Locate every Plasmodium parasite.
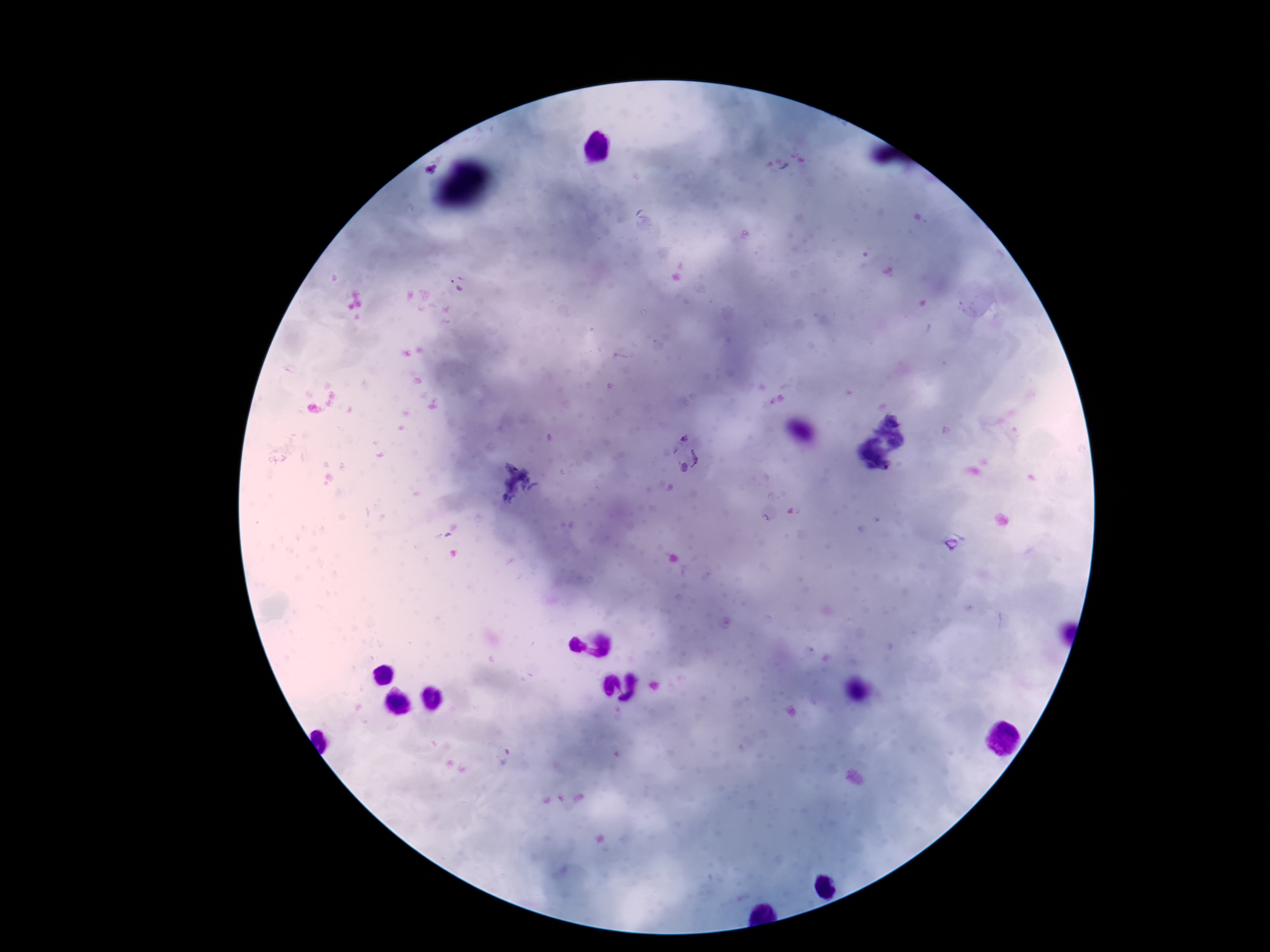
Approximate centers as [x, y] in pixels.
Plasmodium parasites: [429, 169], [459, 285], [685, 455], [952, 544], [504, 755].

One field from this slide. 100x magnification. Thick blood film. Patient malaria status: infected. Image is 1270×952 pixels. Giemsa-stained preparation. Photographed through the microscope eyepiece with a smartphone camera.